Give the extent of all Plasmodium falciparum-infected red blood cells.
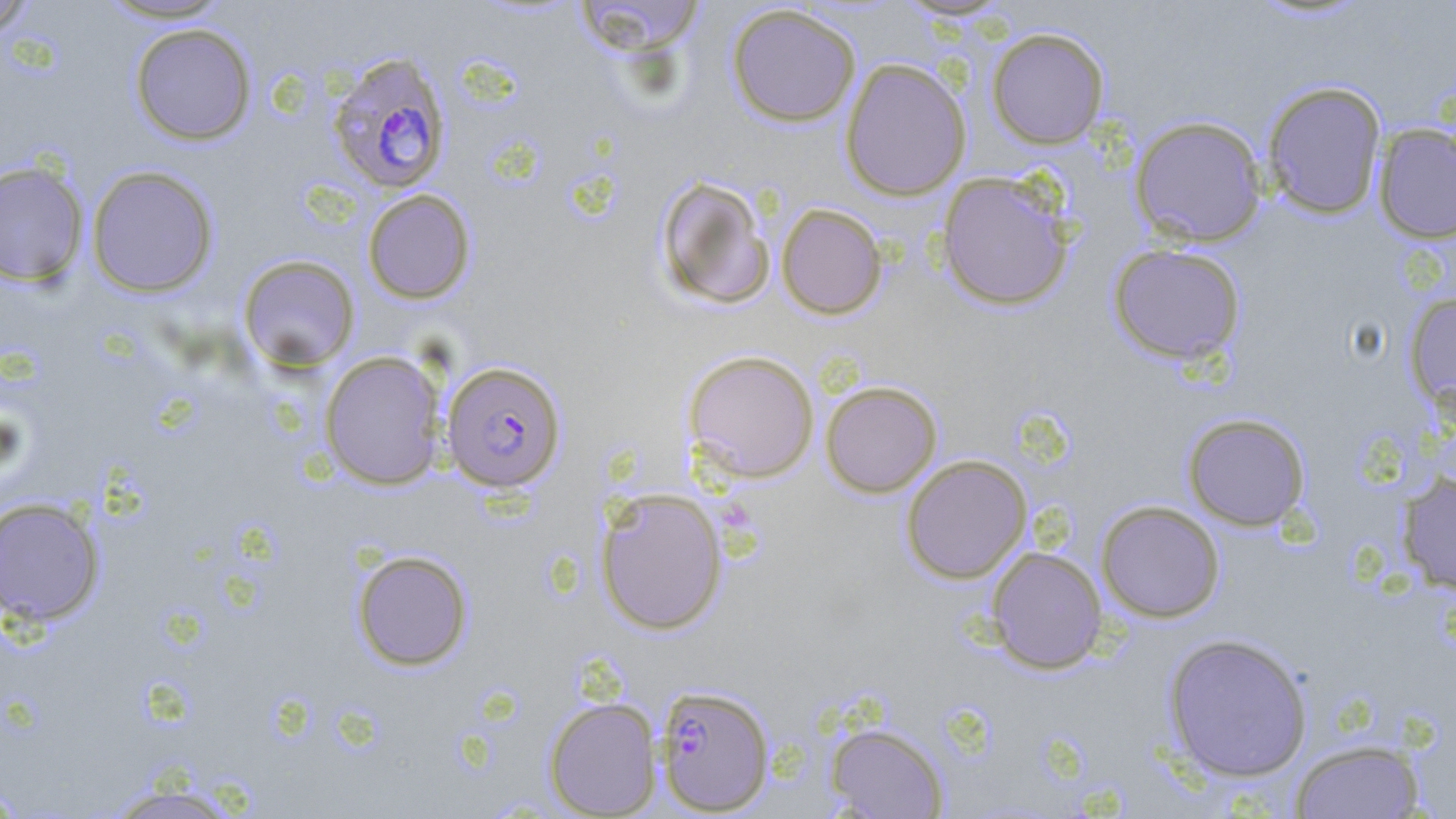

Approximate bounding boxes as (x1, y1, x2, y2) in pixels.
Plasmodium falciparum-infected red blood cells: (327, 52, 452, 195), (441, 361, 566, 493), (655, 684, 775, 815).

slide-level diagnosis = Plasmodium falciparum
modality = light microscopy
field of view = one of a larger specimen
stain = May-Grünwald-Giemsa
preparation = thin blood smear
image size = 1456×819 pixels
uninfected red blood cell locations = approximate bounding boxes as (x1, y1, x2, y2) in pixels: (0, 0, 37, 37), (94, 0, 239, 24), (571, 0, 706, 56), (726, 4, 861, 127), (129, 23, 257, 145), (986, 27, 1109, 149), (840, 58, 971, 201), (1261, 80, 1387, 219), (1129, 115, 1267, 247), (1373, 123, 1456, 245), (0, 160, 89, 287), (86, 165, 219, 298), (936, 172, 1074, 312), (653, 175, 777, 311), (362, 189, 475, 304), (776, 203, 888, 320), (1108, 243, 1246, 365), (238, 254, 360, 372), (1404, 291, 1456, 415), (683, 349, 819, 483), (319, 350, 447, 490), (820, 380, 942, 498), (1182, 413, 1311, 531), (900, 454, 1032, 584), (1398, 471, 1456, 594), (595, 488, 729, 635), (0, 497, 105, 627), (1096, 500, 1225, 623), (986, 546, 1107, 674), (351, 549, 473, 671), (1162, 632, 1314, 782), (544, 697, 661, 817), (825, 722, 949, 818), (1289, 739, 1426, 819), (0, 781, 27, 817), (98, 781, 248, 819)
magnification = 1000x